Report the malaria status of this cell.
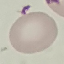

Uninfected.

Summary:
  - Preparation: thin blood film
  - Stain: Giemsa
  - Image type: cell patch, automatically extracted from a larger field of view and resized to 64 × 64 pixels
  - Capture: smartphone camera at the microscope eyepiece